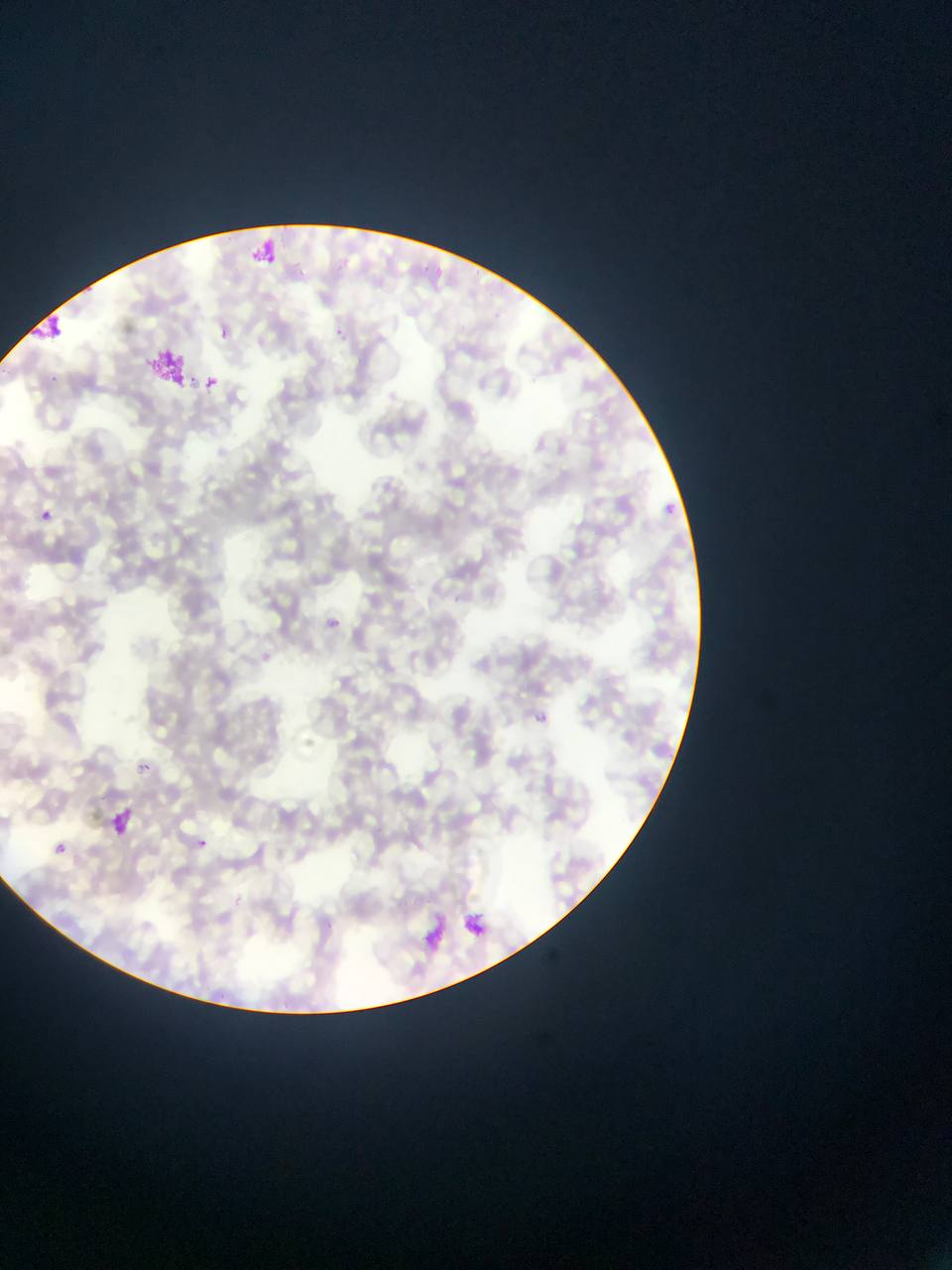 Approximate bounding boxes as (left, top, right, bottom) in pixels. Plasmodium parasite locations: (425, 262, 442, 279), (335, 263, 352, 276), (336, 323, 353, 344), (217, 325, 232, 337), (46, 373, 59, 391), (187, 373, 197, 387), (206, 377, 218, 388), (665, 498, 679, 517), (40, 509, 51, 520), (328, 614, 345, 633), (535, 712, 548, 725), (140, 763, 150, 772), (110, 805, 138, 835), (198, 840, 207, 849), (54, 843, 67, 854), (459, 909, 490, 945). Artifact (stain precipitate or debris) locations: (239, 232, 279, 265), (31, 309, 71, 344), (147, 343, 183, 385). Photographed through a microscope with a mobile-phone camera. Image is 952×1270 pixels. Collected in Ghana. Thin blood smear. Single field of view.